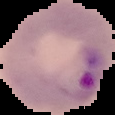

{
  "image_type": "cell region segmented out of the field of view; surrounding area masked to black",
  "image_size": "115×115 pixels",
  "preparation": "thin blood smear",
  "result": "Plasmodium parasites identified"
}